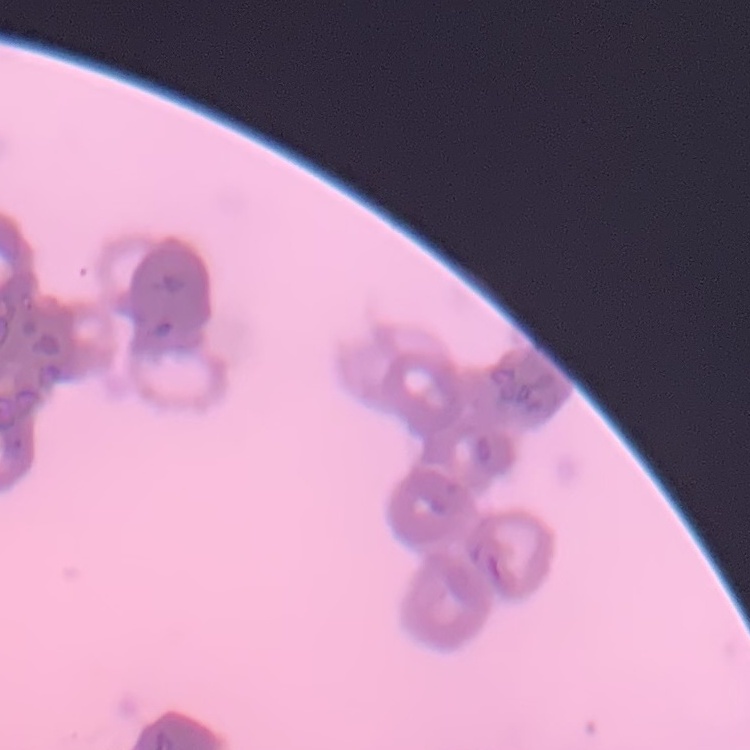

erythrocyte_morphology: rouleaux formation
stain: Field's or Giemsa
image_type: square crop of a larger photomicrograph
preparation: thin blood film